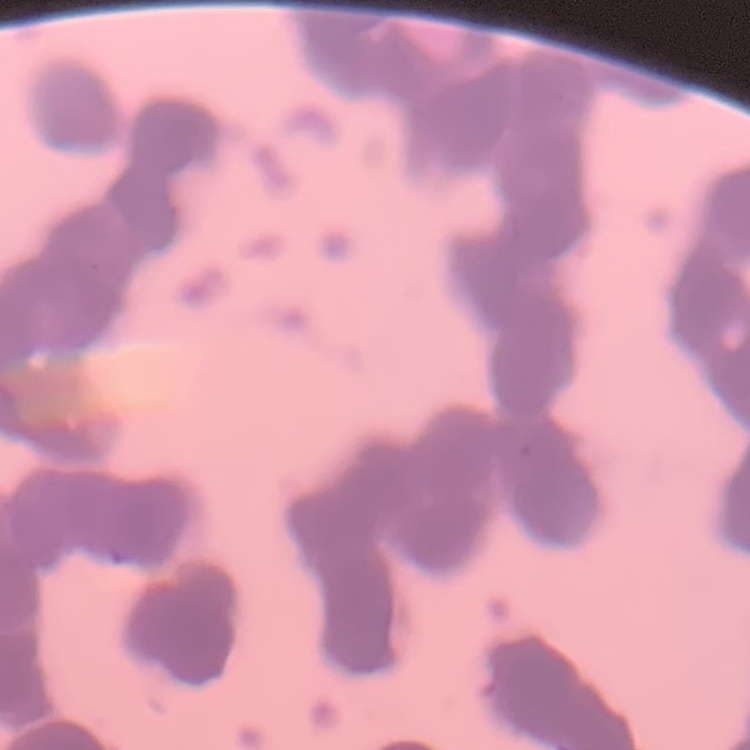

red blood cell morphology = rouleaux formation
stain = Field's or Giemsa
image type = square crop of a larger photomicrograph
preparation = thin blood smear